Outline each blood parasite and name the species.
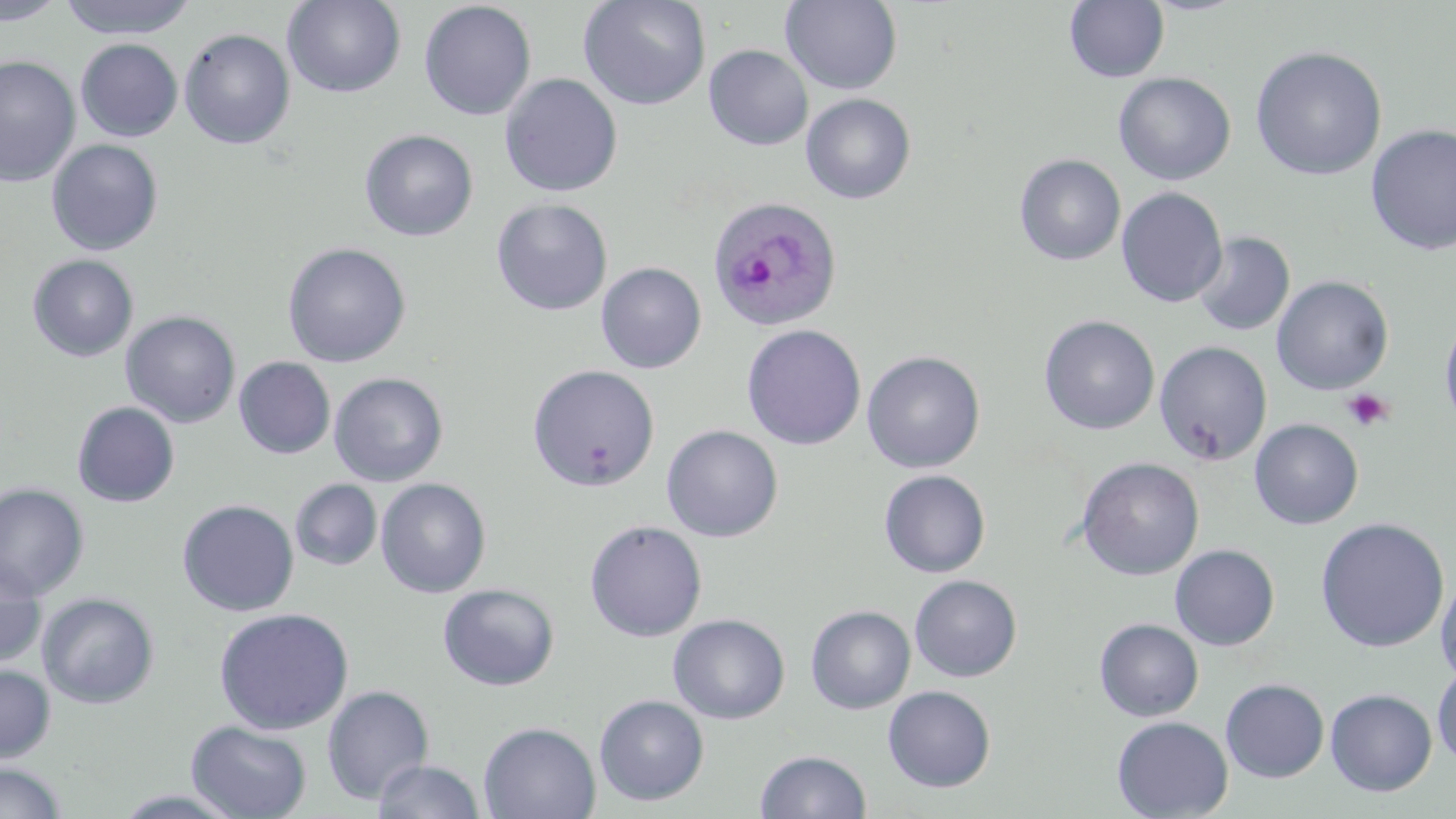
Approximate bounding boxes as (x1, y1, x2, y2) in pixels.
Plasmodium ovale-infected red blood cells: (707, 196, 842, 331).
No Plasmodium falciparum, Plasmodium malariae, Plasmodium vivax, Babesia divergens, or Trypanosoma brucei observed.

Uninfected red blood cell locations: (1, 0, 66, 25), (58, 0, 198, 39), (578, 0, 711, 110), (781, 0, 903, 95), (283, 1, 406, 98), (418, 1, 537, 121), (1064, 1, 1169, 83), (178, 28, 295, 150), (76, 38, 183, 142), (703, 44, 813, 150), (1250, 46, 1387, 181), (0, 55, 81, 188), (1113, 72, 1236, 185), (500, 73, 623, 197), (801, 93, 917, 204), (1365, 124, 1456, 256), (359, 129, 479, 242), (47, 139, 164, 256), (1014, 154, 1126, 266), (1116, 187, 1228, 308), (491, 198, 613, 316), (1192, 231, 1295, 337), (282, 242, 411, 367), (27, 254, 139, 362), (596, 262, 707, 374), (1271, 275, 1394, 395), (121, 310, 241, 428), (1439, 312, 1456, 434), (1039, 315, 1160, 435), (741, 324, 866, 450), (1154, 341, 1272, 466), (861, 350, 985, 473), (234, 356, 336, 459), (527, 364, 660, 492), (328, 372, 449, 487), (72, 402, 180, 507), (1249, 419, 1363, 529), (661, 424, 784, 542), (1075, 457, 1204, 581), (879, 469, 990, 578), (375, 478, 491, 598), (290, 479, 383, 571), (0, 482, 89, 601), (177, 499, 299, 617), (1315, 517, 1450, 653), (584, 520, 707, 641), (1170, 544, 1279, 650), (0, 555, 46, 670), (1435, 570, 1456, 685), (909, 575, 1022, 682), (437, 583, 560, 691), (36, 591, 160, 709), (806, 605, 915, 714), (213, 607, 355, 735), (668, 613, 790, 724), (1094, 618, 1204, 721), (1432, 663, 1456, 768), (0, 664, 56, 764), (1220, 678, 1329, 782), (322, 685, 434, 804), (883, 685, 996, 792), (1325, 688, 1437, 796), (594, 694, 710, 806), (1111, 715, 1233, 818), (186, 720, 312, 818), (478, 721, 600, 819), (755, 749, 872, 819), (371, 759, 486, 818), (0, 761, 66, 819). Platelet locations: (1342, 388, 1394, 433). Slide-level diagnosis: Plasmodium ovale. 1000x magnification. Single field of view. Optical microscopy. Thin blood film. Image is 1456×819 pixels. May-Grünwald-Giemsa stain.